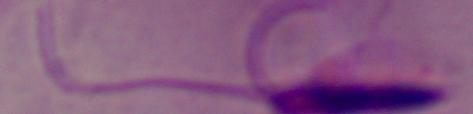
identification = Leishmania
modality = photomicrograph
magnification = 1000x